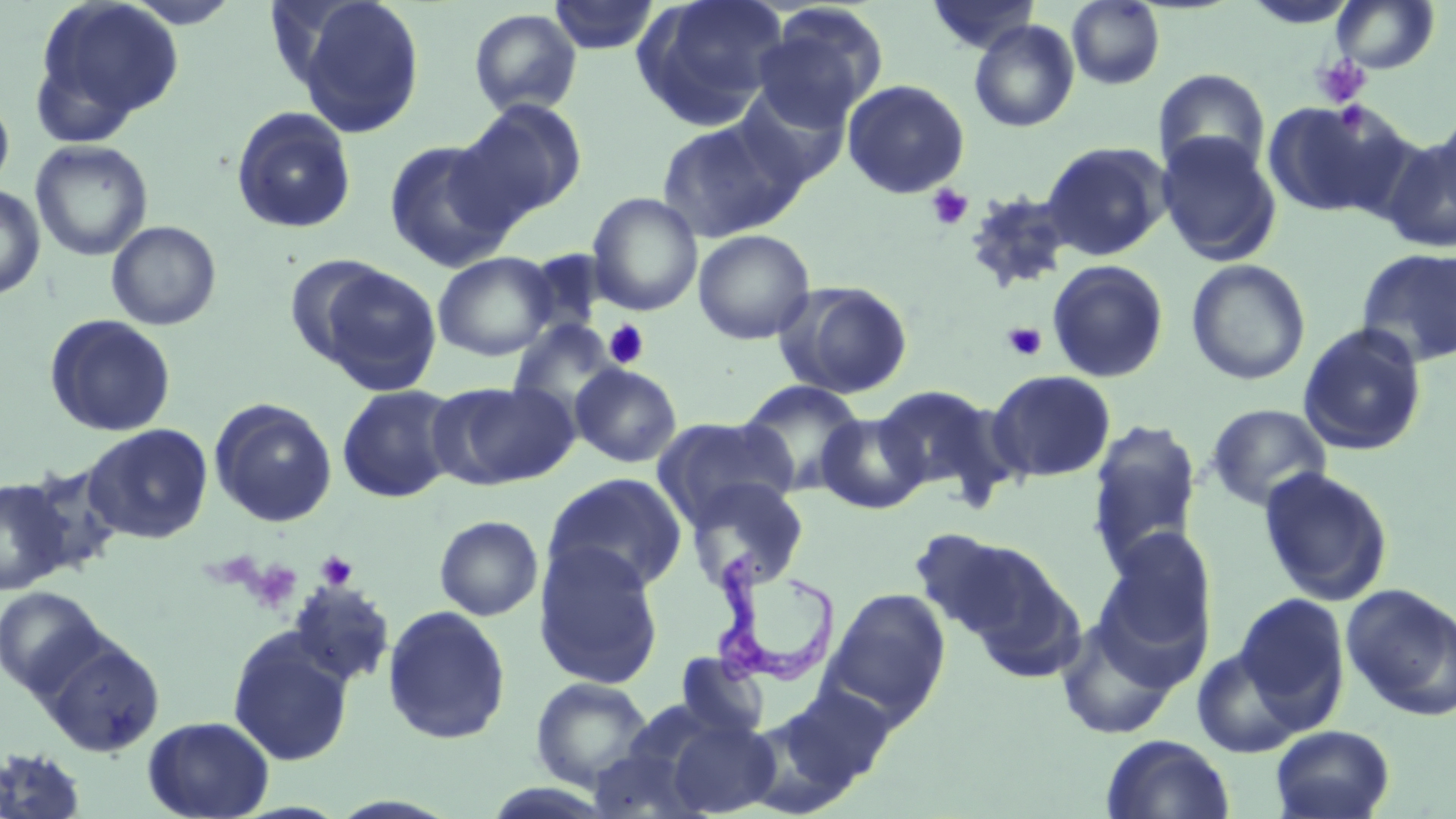 Approximate bounding boxes as (x1, y1, x2, y2) in pixels. Trypanosoma brucei locations: (711, 547, 841, 685). Platelet locations: (1313, 54, 1372, 108), (926, 184, 974, 231), (604, 320, 650, 370), (1002, 322, 1047, 362), (316, 551, 358, 590), (249, 560, 302, 612). Uninfected red blood cell locations: (32, 0, 185, 138), (123, 0, 242, 28), (290, 0, 425, 137), (549, 0, 660, 54), (635, 0, 788, 128), (925, 0, 1041, 55), (1241, 0, 1361, 29), (1330, 0, 1440, 74), (1067, 1, 1165, 89), (751, 7, 886, 132), (469, 8, 582, 117), (969, 20, 1080, 133), (1153, 68, 1271, 179), (841, 78, 970, 199), (731, 83, 852, 190), (0, 91, 15, 195), (1261, 98, 1409, 218), (457, 99, 587, 223), (230, 106, 358, 235), (1433, 110, 1456, 217), (657, 118, 799, 242), (1155, 132, 1282, 266), (1378, 134, 1456, 254), (383, 138, 516, 272), (30, 140, 154, 262), (1040, 141, 1171, 261), (0, 184, 46, 301), (961, 191, 1076, 293), (587, 192, 703, 316), (106, 220, 221, 331), (692, 228, 816, 345), (1355, 247, 1456, 368), (517, 250, 612, 340), (432, 252, 558, 361), (284, 254, 393, 365), (1186, 258, 1311, 385), (1046, 259, 1169, 383), (314, 263, 443, 396), (776, 281, 914, 399), (44, 314, 176, 437), (506, 319, 621, 417), (1298, 323, 1429, 456), (570, 363, 682, 468), (986, 369, 1116, 483), (432, 380, 578, 490), (738, 380, 866, 495), (337, 384, 460, 503), (872, 384, 1008, 499), (209, 398, 338, 527), (1205, 404, 1331, 512), (816, 413, 929, 514), (654, 416, 799, 529), (1086, 418, 1203, 573), (83, 424, 213, 543), (19, 462, 126, 575), (1257, 466, 1394, 606), (542, 473, 688, 595), (0, 476, 75, 595), (684, 478, 809, 592), (434, 515, 543, 621), (1099, 527, 1217, 655), (906, 528, 1048, 647), (533, 542, 666, 690), (944, 543, 1085, 680), (287, 581, 395, 687), (1341, 583, 1456, 721), (0, 585, 112, 702), (821, 587, 952, 727), (1235, 594, 1349, 723), (382, 605, 511, 745), (1055, 617, 1181, 741), (227, 631, 355, 767), (39, 633, 165, 758), (1191, 646, 1306, 758), (672, 654, 771, 744), (529, 676, 655, 791), (762, 682, 897, 804), (660, 712, 781, 817), (143, 715, 274, 818), (1270, 725, 1395, 819), (1100, 734, 1235, 819), (586, 744, 714, 818), (0, 745, 89, 818). Slide-level diagnosis: Trypanosoma brucei. One field of a larger specimen. Image is 1456×819 pixels. Light microscopy. Thin blood film. 1000x magnification. May-Grünwald-Giemsa-stained preparation.